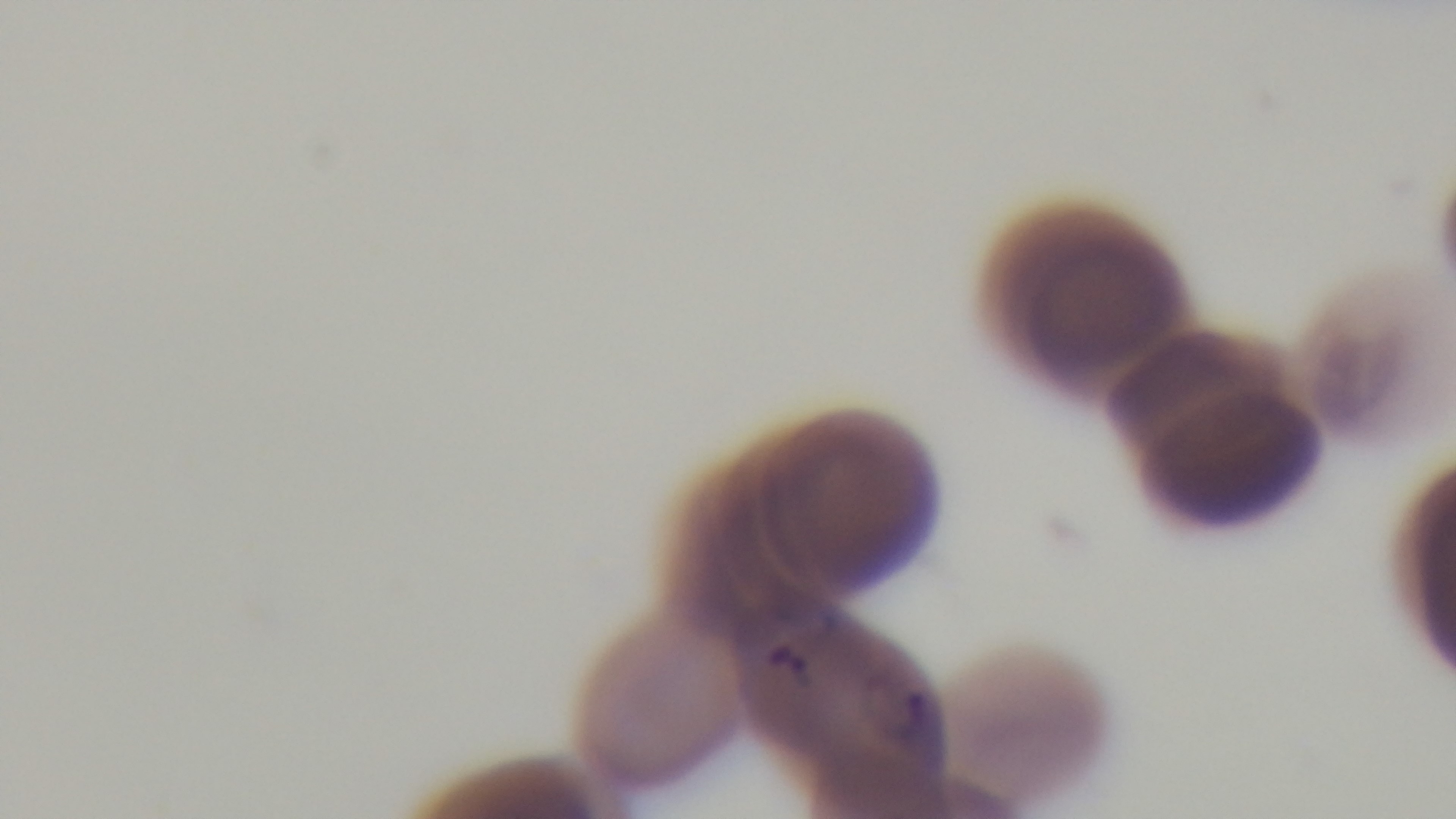
Summary:
  - Modality: light microscopy
  - Capture: mounted 4K digital camera
  - Stain: Giemsa
  - Preparation: thin blood film
  - Malaria status: infected
  - Objective: 100x oil immersion
  - Field of view: single